Comment on the morphology of the erythrocytes.
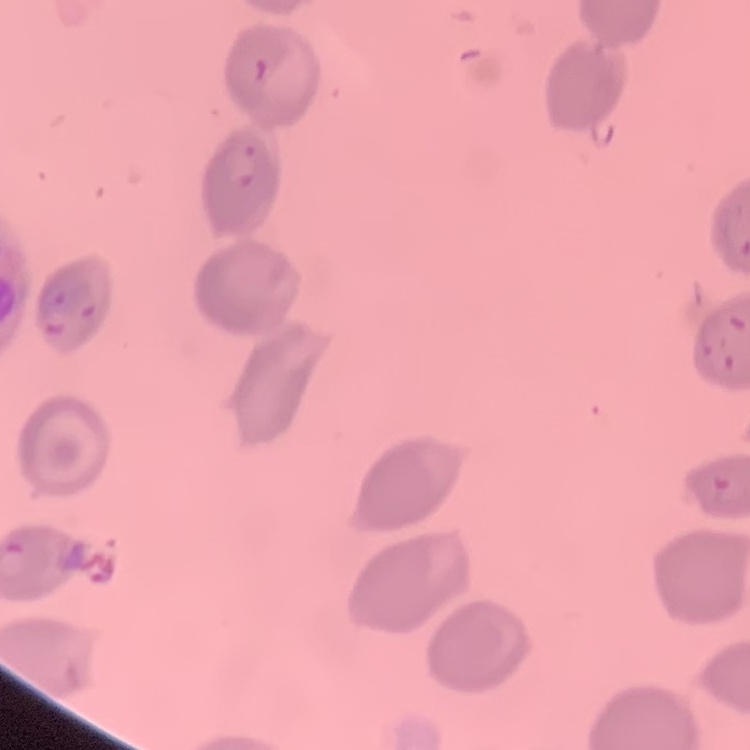

No rouleaux formation.

image type = one tile cut from a larger photomicrograph
preparation = thin blood smear
stain = Field's or Giemsa